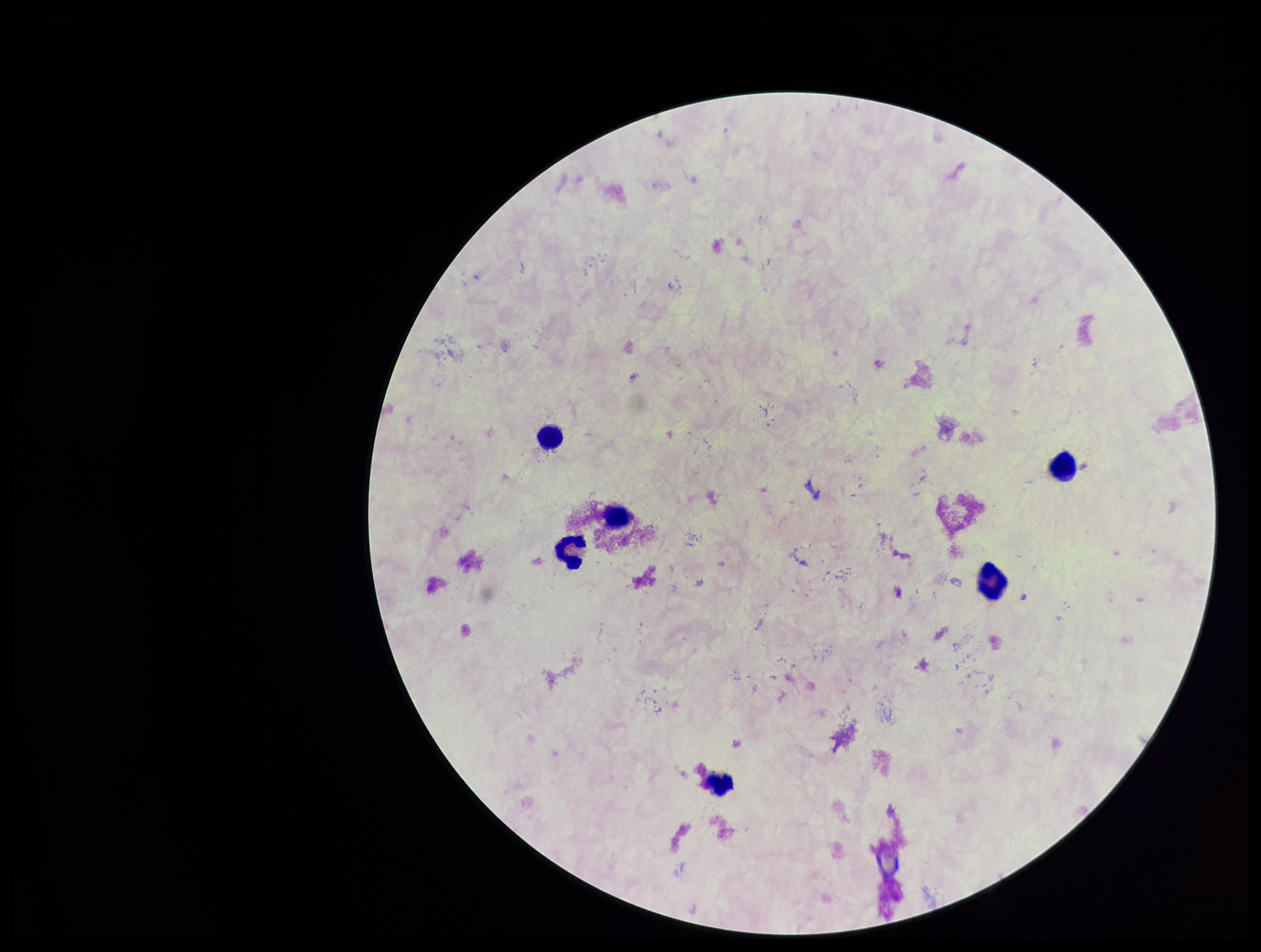

Summary:
  - Preparation: thick smear
  - Image size: 1261×952 pixels
  - Leukocyte count: 6
  - Stain: Giemsa
  - Patient malaria status: negative
  - Capture: smartphone photograph through the microscope eyepiece
  - Parasite count: 0
  - Field of view: one from this slide
  - Plasmodium parasites: none identified